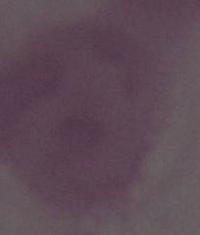
{
  "magnification": "1000x",
  "identification": "erythrocyte",
  "modality": "photomicrograph"
}